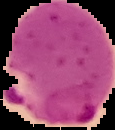
Summary:
  - Image type: cell region segmented out of the field of view; surrounding area masked to black
  - Preparation: thin blood smear
  - Result: Plasmodium parasites identified
  - Image size: 115×130 pixels